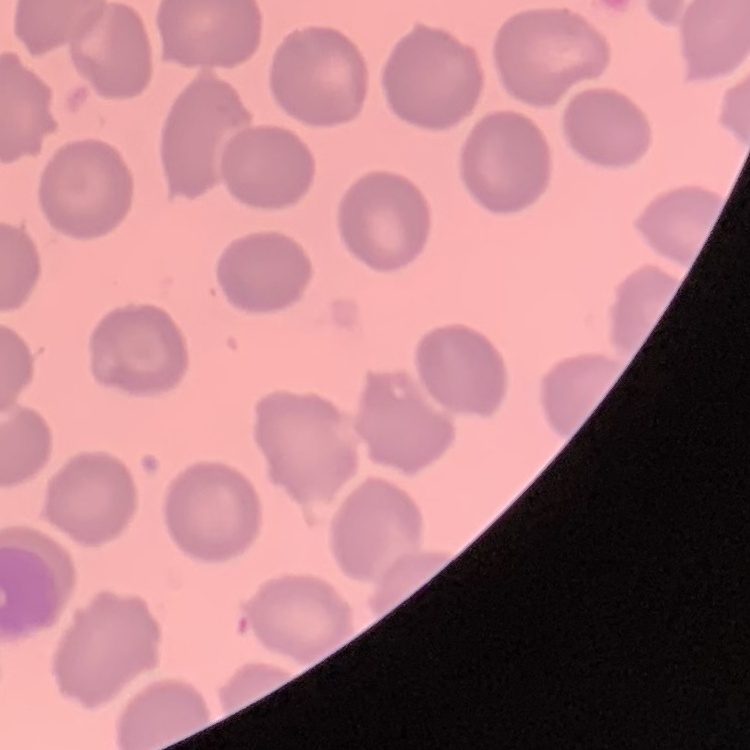
red blood cell morphology = no rouleaux formation
preparation = thin blood film
image type = square crop of a larger photomicrograph
stain = Field's or Giemsa